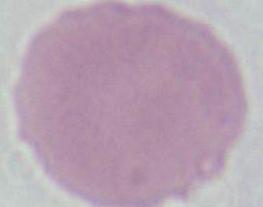
An erythrocyte is seen. Micrograph. Captured at 1000x magnification.